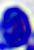
Captured at 400x magnification. Photomicrograph. A white blood cell is seen.